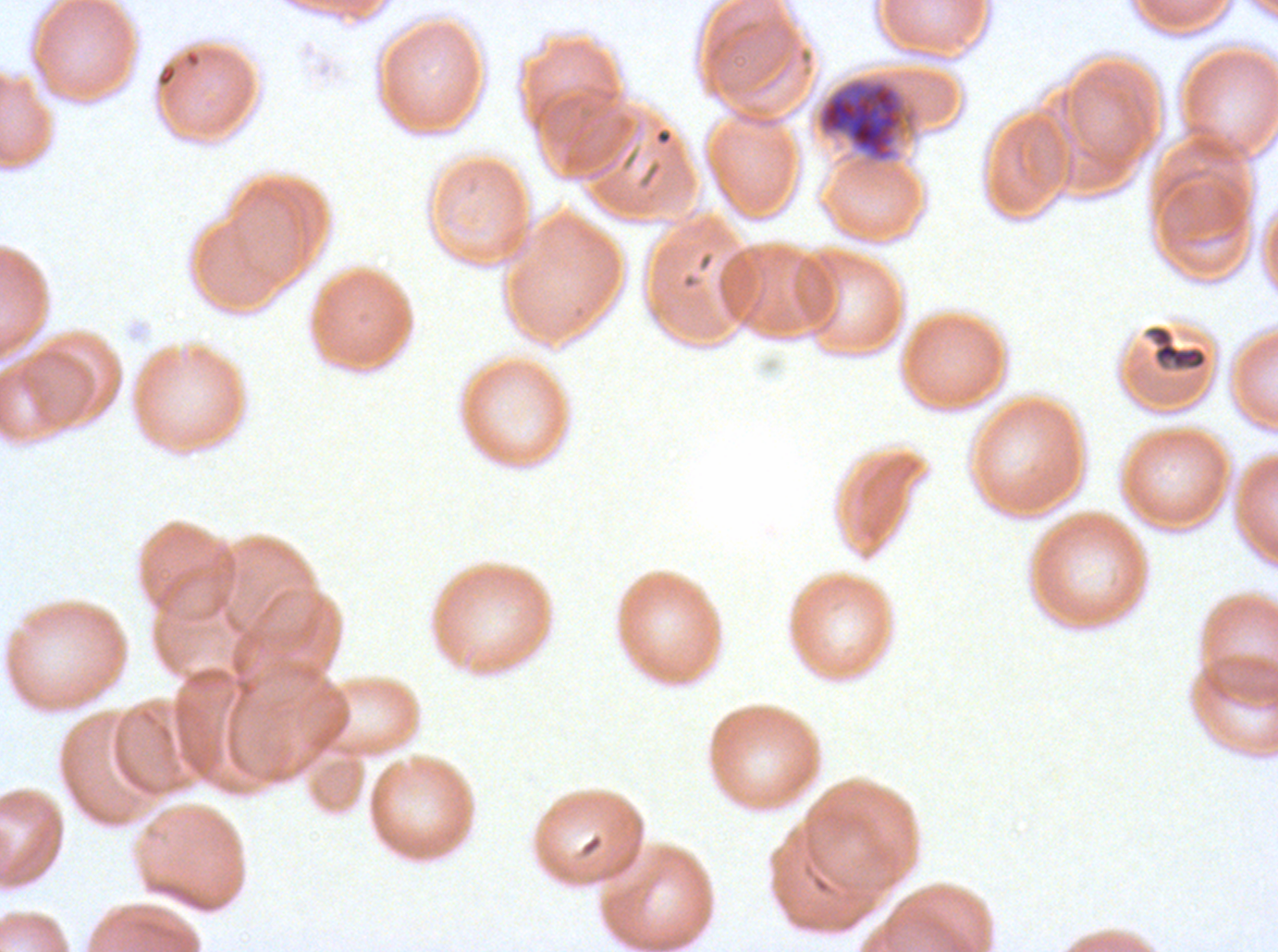

{
  "stain": "Giemsa",
  "field_of_view": "sub-image separated from a larger composite",
  "preparation": "thin blood smear",
  "early_schizont_locations": "approximate bounding boxes as (x1, y1, x2, y2) in pixels: (816, 76, 920, 165)",
  "debris_locations": "approximate bounding boxes as (x1, y1, x2, y2) in pixels: (1144, 324, 1209, 372)",
  "specimen": "ex-vivo Plasmodium falciparum culture from a patient in The Gambia, grown for 24 to 48 hours",
  "image_size": "1278×952 pixels"
}